Locate every blood parasite and identify its species.
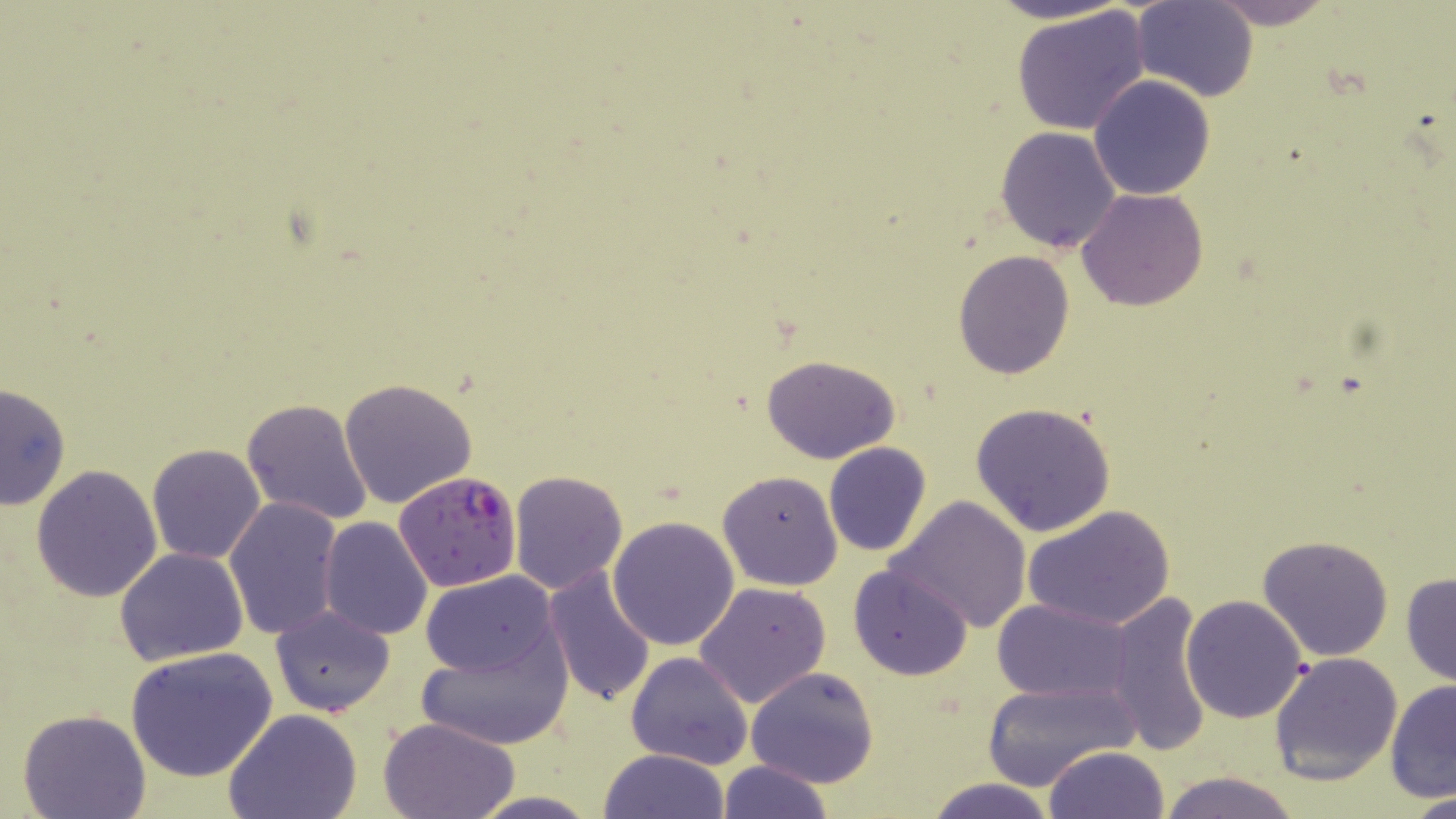
Approximate bounding boxes as named x1/y1/x2/y2 corners in pixels.
Plasmodium falciparum-infected red blood cells: (x1=392, y1=471, x2=522, y2=593).
No Plasmodium ovale, Plasmodium malariae, Plasmodium vivax, Babesia divergens, or Trypanosoma brucei observed.

{
  "slide_level_diagnosis": "Plasmodium falciparum",
  "field_of_view": "one of a larger specimen",
  "modality": "light microscopy",
  "magnification": "1000x",
  "image_size": "1456×819 pixels",
  "uninfected_red_blood_cell_locations": "approximate bounding boxes as named x1/y1/x2/y2 corners in pixels: (x1=979, y1=0, x2=1136, y2=25), (x1=1205, y1=0, x2=1338, y2=29), (x1=1132, y1=1, x2=1257, y2=101), (x1=1010, y1=5, x2=1153, y2=136), (x1=1087, y1=75, x2=1216, y2=201), (x1=994, y1=126, x2=1122, y2=254), (x1=1077, y1=189, x2=1209, y2=312), (x1=953, y1=249, x2=1075, y2=378), (x1=760, y1=352, x2=903, y2=464), (x1=339, y1=376, x2=479, y2=508), (x1=0, y1=380, x2=71, y2=510), (x1=242, y1=398, x2=376, y2=527), (x1=970, y1=401, x2=1117, y2=539), (x1=823, y1=441, x2=932, y2=557), (x1=146, y1=443, x2=266, y2=565), (x1=30, y1=464, x2=162, y2=603), (x1=717, y1=469, x2=843, y2=591), (x1=509, y1=470, x2=627, y2=593), (x1=885, y1=495, x2=1033, y2=634), (x1=225, y1=496, x2=342, y2=641), (x1=1022, y1=504, x2=1176, y2=631), (x1=608, y1=515, x2=742, y2=650), (x1=319, y1=517, x2=433, y2=640), (x1=1258, y1=534, x2=1395, y2=661), (x1=114, y1=547, x2=248, y2=667), (x1=848, y1=563, x2=975, y2=681), (x1=542, y1=567, x2=657, y2=708), (x1=421, y1=571, x2=560, y2=680), (x1=1400, y1=572, x2=1456, y2=687), (x1=694, y1=582, x2=831, y2=708), (x1=1102, y1=592, x2=1216, y2=756), (x1=1181, y1=594, x2=1308, y2=723), (x1=992, y1=598, x2=1135, y2=703), (x1=270, y1=604, x2=397, y2=717), (x1=415, y1=630, x2=574, y2=752), (x1=124, y1=647, x2=278, y2=782), (x1=1268, y1=650, x2=1403, y2=786), (x1=624, y1=652, x2=754, y2=770), (x1=744, y1=667, x2=879, y2=789), (x1=981, y1=676, x2=1137, y2=789), (x1=1384, y1=682, x2=1456, y2=803), (x1=17, y1=707, x2=150, y2=818), (x1=223, y1=709, x2=363, y2=819), (x1=378, y1=716, x2=521, y2=819), (x1=1044, y1=746, x2=1169, y2=819), (x1=598, y1=748, x2=731, y2=819), (x1=716, y1=759, x2=835, y2=819), (x1=1154, y1=770, x2=1302, y2=819), (x1=926, y1=777, x2=1059, y2=819), (x1=1406, y1=791, x2=1456, y2=819), (x1=467, y1=792, x2=601, y2=818)",
  "stain": "May-Grünwald-Giemsa",
  "preparation": "thin blood smear"
}